Outline each blood parasite and name the species.
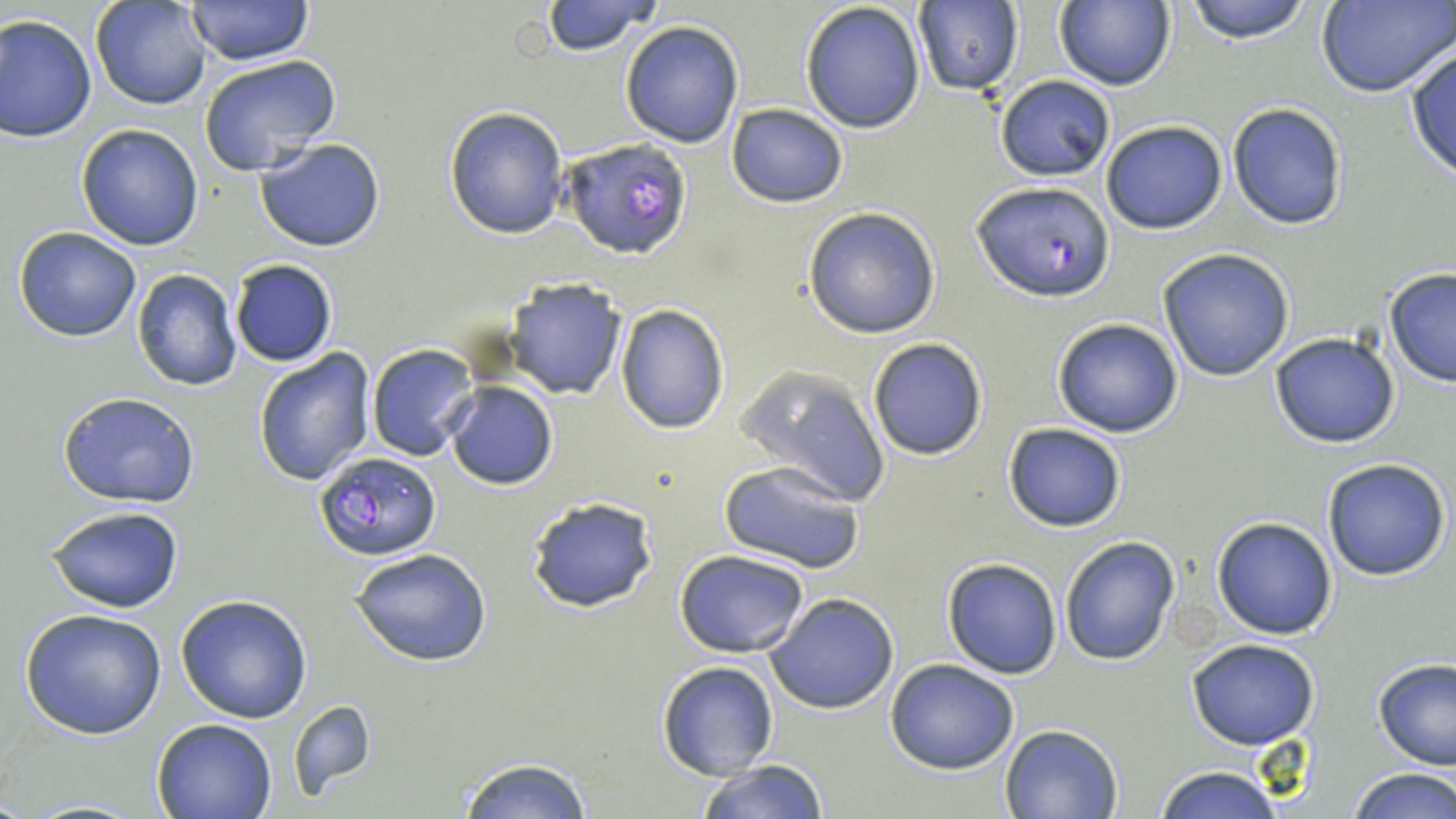
Approximate bounding boxes as (x1,y1)-(x2,y2) corner pairs in pixels.
Plasmodium falciparum-infected red blood cells: (559,138)-(693,261), (974,181)-(1114,301), (314,450)-(442,560).
No Plasmodium ovale, Plasmodium malariae, Plasmodium vivax, Babesia divergens, or Trypanosoma brucei observed.

Summary:
  - Uninfected red blood cell locations: (92,0)-(213,110), (539,0)-(664,55), (1180,0)-(1317,44), (186,1)-(312,67), (1054,1)-(1175,91), (914,2)-(1023,95), (1317,2)-(1455,98), (800,3)-(927,134), (0,15)-(97,142), (621,20)-(745,147), (1404,48)-(1456,181), (197,55)-(341,176), (994,75)-(1117,181), (1227,101)-(1348,231), (725,102)-(849,207), (443,105)-(569,240), (1101,119)-(1229,234), (76,125)-(203,249), (254,137)-(386,253), (803,206)-(943,339), (13,227)-(141,343), (1157,247)-(1295,381), (228,259)-(338,368), (132,269)-(243,392), (1384,269)-(1456,385), (502,277)-(627,399), (615,305)-(729,434), (1051,317)-(1184,438), (1268,331)-(1400,449), (866,337)-(990,461), (366,344)-(480,461), (255,349)-(380,489), (738,366)-(888,508), (443,381)-(558,490), (57,391)-(200,507), (1002,423)-(1127,532), (1322,457)-(1451,581), (717,458)-(867,572), (525,495)-(658,613), (46,504)-(186,613), (1212,515)-(1338,639), (1059,537)-(1179,667), (352,547)-(493,667), (676,550)-(810,658), (942,558)-(1064,678), (765,593)-(898,715), (175,595)-(313,723), (21,608)-(168,739), (1188,640)-(1320,750), (1373,657)-(1456,770), (885,658)-(1020,775), (657,661)-(780,781), (289,698)-(376,797), (150,717)-(276,819), (1000,723)-(1124,818), (455,756)-(594,818), (694,759)-(830,818), (1152,765)-(1283,819), (1346,768)-(1456,819), (16,798)-(153,818)
  - Slide-level diagnosis: Plasmodium falciparum
  - Field of view: one of a larger specimen
  - Stain: May-Grünwald-Giemsa
  - Magnification: 1000x
  - Preparation: thin blood smear
  - Modality: optical microscopy
  - Image size: 1456×819 pixels